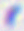
Micrograph. Captured at 400x magnification. Toxoplasma gondii is shown.